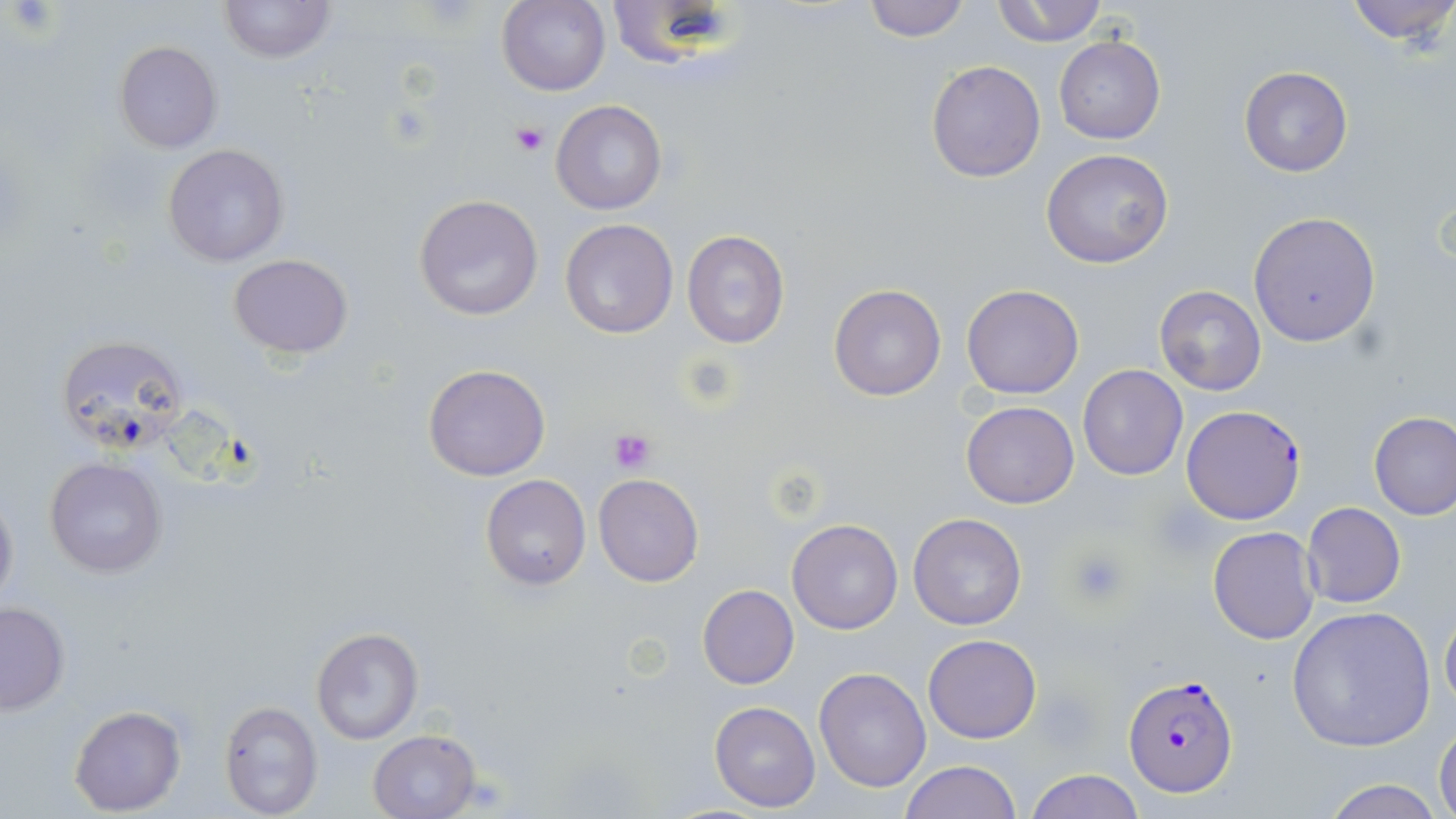
Approximate bounding boxes as named x1/y1/x2/y2 corners in pixels. Plasmodium falciparum-infected red blood cell locations: (x1=1183, y1=403, x2=1309, y2=522), (x1=1124, y1=678, x2=1236, y2=802). Platelet locations: (x1=510, y1=123, x2=549, y2=156), (x1=608, y1=428, x2=657, y2=473), (x1=1067, y1=548, x2=1128, y2=606). Uninfected red blood cell locations: (x1=220, y1=0, x2=333, y2=63), (x1=605, y1=0, x2=739, y2=69), (x1=860, y1=0, x2=972, y2=42), (x1=991, y1=0, x2=1108, y2=47), (x1=1341, y1=0, x2=1456, y2=45), (x1=498, y1=1, x2=610, y2=97), (x1=1053, y1=36, x2=1166, y2=144), (x1=114, y1=40, x2=222, y2=153), (x1=926, y1=60, x2=1046, y2=182), (x1=1239, y1=66, x2=1353, y2=177), (x1=552, y1=101, x2=667, y2=216), (x1=162, y1=145, x2=289, y2=265), (x1=1041, y1=148, x2=1173, y2=268), (x1=413, y1=194, x2=545, y2=321), (x1=1248, y1=212, x2=1380, y2=346), (x1=559, y1=217, x2=678, y2=338), (x1=682, y1=230, x2=790, y2=348), (x1=229, y1=253, x2=354, y2=357), (x1=828, y1=282, x2=948, y2=402), (x1=961, y1=283, x2=1084, y2=399), (x1=1154, y1=285, x2=1268, y2=396), (x1=54, y1=334, x2=188, y2=456), (x1=423, y1=364, x2=550, y2=481), (x1=1077, y1=364, x2=1187, y2=481), (x1=960, y1=401, x2=1079, y2=509), (x1=1369, y1=411, x2=1456, y2=521), (x1=43, y1=456, x2=168, y2=579), (x1=593, y1=473, x2=705, y2=587), (x1=480, y1=475, x2=592, y2=590), (x1=0, y1=487, x2=19, y2=617), (x1=1302, y1=502, x2=1406, y2=608), (x1=908, y1=512, x2=1027, y2=630), (x1=787, y1=519, x2=902, y2=634), (x1=1207, y1=526, x2=1320, y2=644), (x1=696, y1=584, x2=800, y2=689), (x1=0, y1=601, x2=70, y2=714), (x1=1440, y1=601, x2=1456, y2=718), (x1=1285, y1=605, x2=1436, y2=751), (x1=310, y1=627, x2=422, y2=745), (x1=923, y1=634, x2=1041, y2=743), (x1=813, y1=667, x2=931, y2=793), (x1=219, y1=701, x2=324, y2=818), (x1=710, y1=701, x2=820, y2=811), (x1=69, y1=705, x2=186, y2=815), (x1=1434, y1=722, x2=1456, y2=819), (x1=368, y1=730, x2=480, y2=818), (x1=899, y1=761, x2=1021, y2=819), (x1=1024, y1=769, x2=1145, y2=819), (x1=1320, y1=778, x2=1443, y2=819). Slide-level diagnosis: Plasmodium falciparum. Captured at 1000x magnification. Image is 1456×819 pixels. May-Grünwald-Giemsa stain. Optical microscopy. Thin blood smear. Single field of view.